Classify this cell by malaria status.
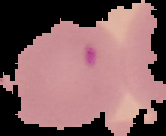
It is parasitized.

From a thin blood smear. Image is 166×136 pixels. Cell region segmented out of the field of view; the surrounding area is masked to black.